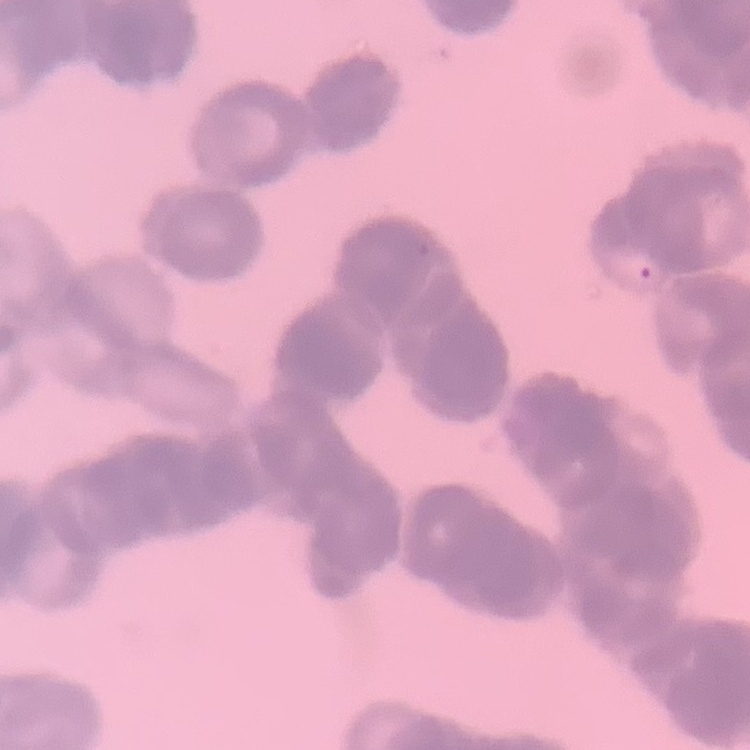

red blood cell morphology = rouleaux formation
stain = Field's or Giemsa
preparation = thin peripheral smear
image type = one tile cut from a larger photomicrograph